Classify this cell by malaria status.
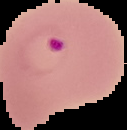

It is parasitized.

Summary:
  - Image size: 127×130 pixels
  - Preparation: thin blood smear
  - Image type: segmented cell region on a black background